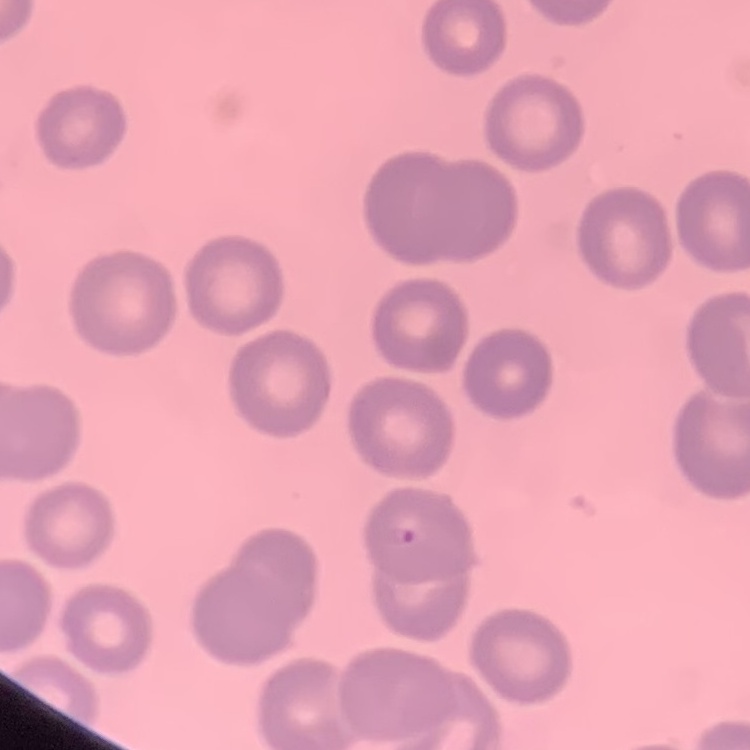

The red blood cells show no rouleaux formation. One tile cut from a larger photomicrograph. Thin blood film. Stained with either Field's or Giemsa.